State which parasite is depicted.
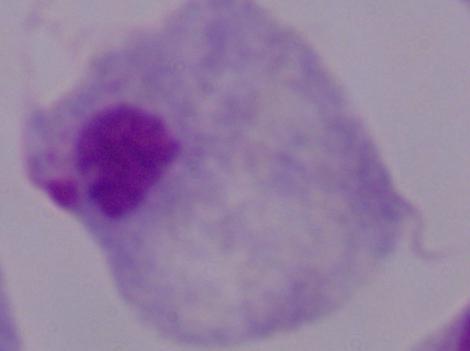

A trichomonad.

Micrograph. 1000x magnification.